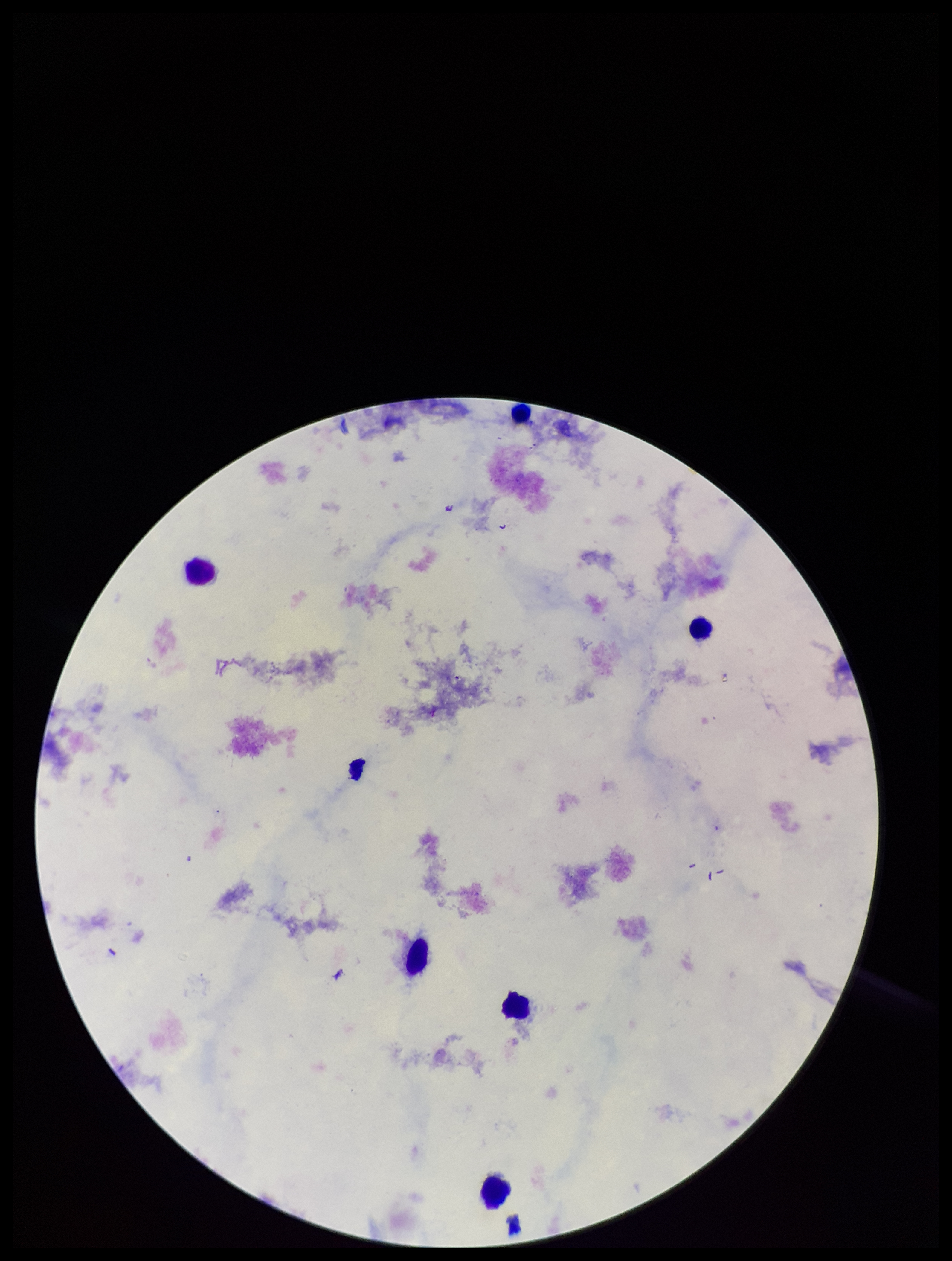

stain = Giemsa
patient malaria status = negative
capture = smartphone photograph through the microscope eyepiece
preparation = thick blood smear
Plasmodium parasites = none identified
field of view = single
leukocyte count = 6
parasite count = 0
image size = 952×1261 pixels